Mark where platelets are.
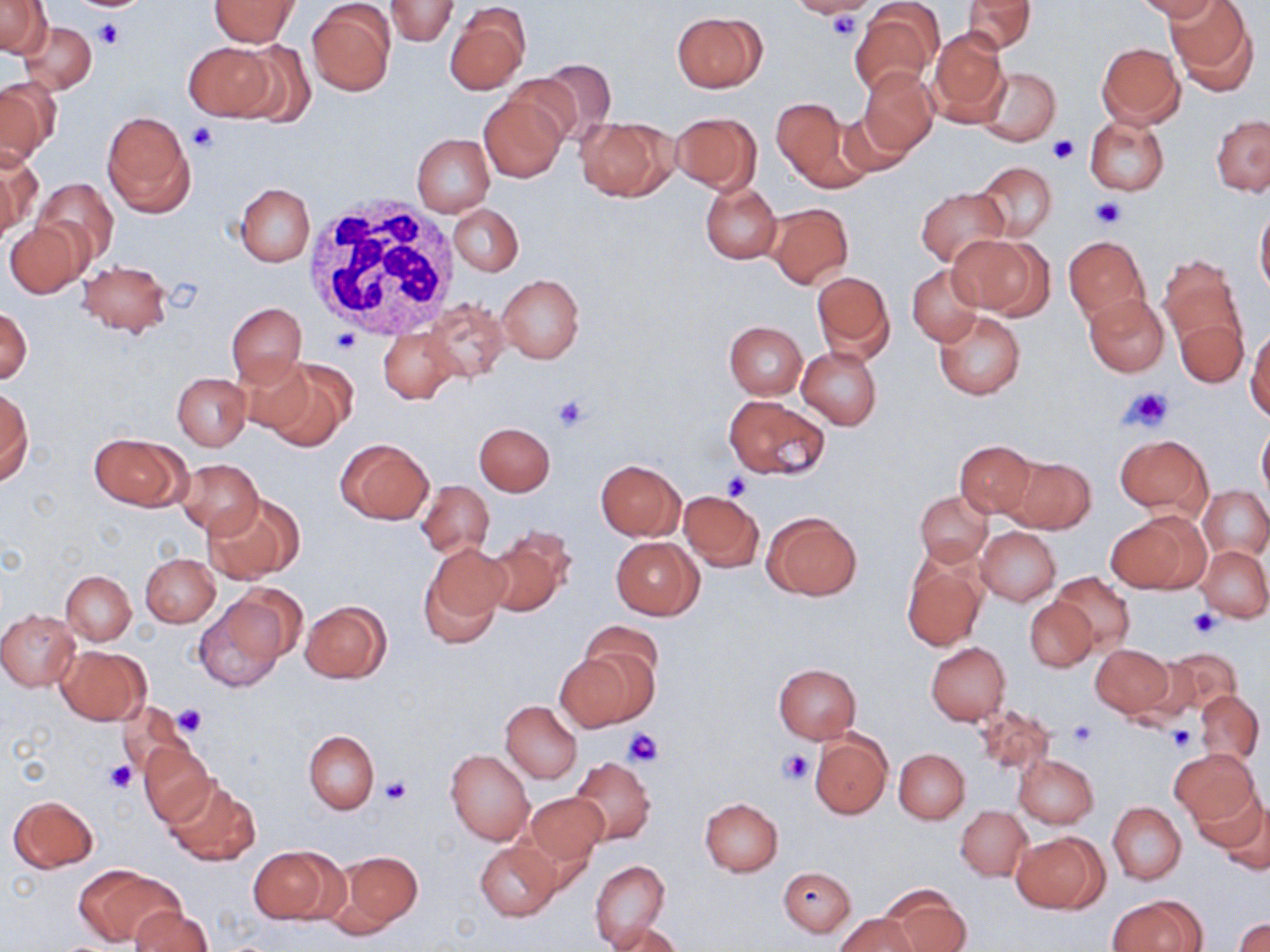

Approximate bounding boxes as named x1/y1/x2/y2 corners in pixels.
Platelets: (x1=77, y1=1, x2=143, y2=12), (x1=825, y1=11, x2=864, y2=42), (x1=95, y1=19, x2=126, y2=50), (x1=187, y1=123, x2=219, y2=153), (x1=1046, y1=137, x2=1078, y2=164), (x1=1088, y1=195, x2=1128, y2=230), (x1=331, y1=329, x2=361, y2=355), (x1=1122, y1=386, x2=1174, y2=432), (x1=550, y1=392, x2=591, y2=432), (x1=723, y1=475, x2=750, y2=501), (x1=1188, y1=608, x2=1222, y2=636), (x1=171, y1=704, x2=207, y2=737), (x1=1067, y1=720, x2=1096, y2=748), (x1=1166, y1=726, x2=1195, y2=755), (x1=623, y1=729, x2=664, y2=765), (x1=778, y1=749, x2=814, y2=785), (x1=105, y1=761, x2=137, y2=794), (x1=380, y1=775, x2=412, y2=806).

Summary:
  - Uninfected red blood cell locations: (x1=0, y1=0, x2=51, y2=58), (x1=209, y1=0, x2=299, y2=46), (x1=385, y1=0, x2=458, y2=47), (x1=797, y1=0, x2=873, y2=19), (x1=852, y1=0, x2=943, y2=97), (x1=963, y1=0, x2=1036, y2=54), (x1=1136, y1=0, x2=1221, y2=21), (x1=1166, y1=0, x2=1257, y2=92), (x1=307, y1=3, x2=396, y2=96), (x1=443, y1=3, x2=530, y2=95), (x1=672, y1=11, x2=766, y2=92), (x1=19, y1=22, x2=98, y2=94), (x1=927, y1=28, x2=1011, y2=126), (x1=184, y1=42, x2=275, y2=120), (x1=230, y1=42, x2=317, y2=125), (x1=1097, y1=42, x2=1184, y2=127), (x1=530, y1=57, x2=618, y2=144), (x1=979, y1=66, x2=1061, y2=145), (x1=858, y1=68, x2=938, y2=158), (x1=0, y1=78, x2=59, y2=165), (x1=478, y1=92, x2=566, y2=182), (x1=772, y1=96, x2=858, y2=187), (x1=833, y1=109, x2=916, y2=180), (x1=102, y1=111, x2=194, y2=218), (x1=670, y1=111, x2=762, y2=193), (x1=1212, y1=115, x2=1270, y2=194), (x1=574, y1=116, x2=678, y2=201), (x1=1085, y1=116, x2=1169, y2=195), (x1=412, y1=134, x2=494, y2=217), (x1=0, y1=149, x2=39, y2=238), (x1=974, y1=161, x2=1058, y2=241), (x1=34, y1=178, x2=119, y2=265), (x1=700, y1=181, x2=782, y2=263), (x1=235, y1=183, x2=315, y2=266), (x1=916, y1=188, x2=1010, y2=268), (x1=448, y1=203, x2=525, y2=278), (x1=765, y1=203, x2=853, y2=290), (x1=1256, y1=203, x2=1270, y2=299), (x1=4, y1=220, x2=87, y2=297), (x1=949, y1=232, x2=1050, y2=318), (x1=1064, y1=236, x2=1151, y2=325), (x1=1159, y1=256, x2=1247, y2=352), (x1=78, y1=260, x2=171, y2=337), (x1=908, y1=265, x2=983, y2=345), (x1=812, y1=271, x2=895, y2=363), (x1=498, y1=274, x2=584, y2=363), (x1=1084, y1=292, x2=1169, y2=376), (x1=423, y1=300, x2=510, y2=382), (x1=226, y1=303, x2=306, y2=388), (x1=1, y1=306, x2=32, y2=385), (x1=934, y1=311, x2=1026, y2=399), (x1=1175, y1=317, x2=1247, y2=387), (x1=724, y1=321, x2=807, y2=399), (x1=1247, y1=327, x2=1270, y2=420), (x1=379, y1=328, x2=461, y2=404), (x1=797, y1=347, x2=881, y2=429), (x1=233, y1=356, x2=317, y2=436), (x1=261, y1=362, x2=355, y2=450), (x1=173, y1=374, x2=249, y2=450), (x1=1, y1=389, x2=32, y2=486), (x1=724, y1=395, x2=829, y2=481), (x1=1257, y1=421, x2=1270, y2=501), (x1=474, y1=422, x2=554, y2=496), (x1=90, y1=433, x2=186, y2=510), (x1=1115, y1=435, x2=1211, y2=515), (x1=335, y1=438, x2=434, y2=524), (x1=954, y1=439, x2=1037, y2=517), (x1=1004, y1=456, x2=1096, y2=534), (x1=174, y1=458, x2=264, y2=538), (x1=595, y1=460, x2=686, y2=540), (x1=417, y1=480, x2=494, y2=559), (x1=1200, y1=486, x2=1270, y2=559), (x1=679, y1=490, x2=765, y2=571), (x1=915, y1=490, x2=992, y2=566), (x1=203, y1=494, x2=304, y2=583), (x1=763, y1=511, x2=862, y2=600), (x1=1107, y1=513, x2=1204, y2=595), (x1=976, y1=526, x2=1061, y2=606), (x1=483, y1=528, x2=575, y2=616), (x1=611, y1=537, x2=703, y2=619), (x1=1197, y1=544, x2=1270, y2=622), (x1=419, y1=545, x2=509, y2=645), (x1=901, y1=553, x2=989, y2=651), (x1=140, y1=554, x2=220, y2=627), (x1=62, y1=570, x2=136, y2=645), (x1=1049, y1=574, x2=1135, y2=653), (x1=193, y1=596, x2=288, y2=691), (x1=1025, y1=597, x2=1096, y2=671), (x1=299, y1=600, x2=391, y2=683), (x1=0, y1=609, x2=79, y2=691), (x1=579, y1=621, x2=663, y2=698), (x1=926, y1=642, x2=1010, y2=724), (x1=1090, y1=643, x2=1175, y2=719), (x1=57, y1=645, x2=149, y2=724), (x1=1156, y1=647, x2=1243, y2=718), (x1=555, y1=651, x2=653, y2=731), (x1=773, y1=664, x2=861, y2=743), (x1=1194, y1=690, x2=1263, y2=765), (x1=501, y1=701, x2=582, y2=783), (x1=972, y1=702, x2=1055, y2=778), (x1=118, y1=703, x2=191, y2=779), (x1=304, y1=730, x2=379, y2=814), (x1=809, y1=730, x2=892, y2=819), (x1=139, y1=742, x2=217, y2=826), (x1=894, y1=748, x2=969, y2=823), (x1=1169, y1=748, x2=1259, y2=826), (x1=447, y1=749, x2=534, y2=845), (x1=1013, y1=754, x2=1098, y2=828), (x1=568, y1=755, x2=656, y2=846), (x1=164, y1=779, x2=260, y2=867), (x1=1195, y1=786, x2=1270, y2=867), (x1=523, y1=792, x2=606, y2=871), (x1=7, y1=794, x2=99, y2=873), (x1=700, y1=797, x2=784, y2=876), (x1=1109, y1=802, x2=1185, y2=885), (x1=956, y1=805, x2=1032, y2=881), (x1=1012, y1=831, x2=1107, y2=913), (x1=475, y1=841, x2=563, y2=921), (x1=248, y1=844, x2=341, y2=926), (x1=329, y1=849, x2=424, y2=935), (x1=590, y1=860, x2=669, y2=951), (x1=75, y1=866, x2=180, y2=947), (x1=778, y1=866, x2=855, y2=936), (x1=880, y1=887, x2=969, y2=952), (x1=1107, y1=895, x2=1202, y2=951), (x1=130, y1=906, x2=213, y2=952), (x1=835, y1=912, x2=917, y2=952), (x1=603, y1=919, x2=681, y2=952), (x1=1234, y1=919, x2=1270, y2=952)
  - White blood cell locations: (x1=307, y1=196, x2=465, y2=338)
  - Slide-level diagnosis: no evidence of blood parasites
  - Field of view: single
  - Modality: light microscopy
  - Magnification: 1000x
  - Stain: May-Grünwald-Giemsa
  - Preparation: thin blood film
  - Image size: 1270×952 pixels